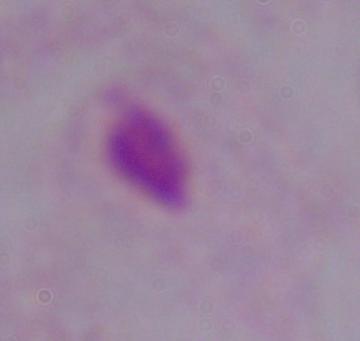

Summary:
  - Modality: photomicrograph
  - Identification: trichomonad
  - Magnification: 1000x